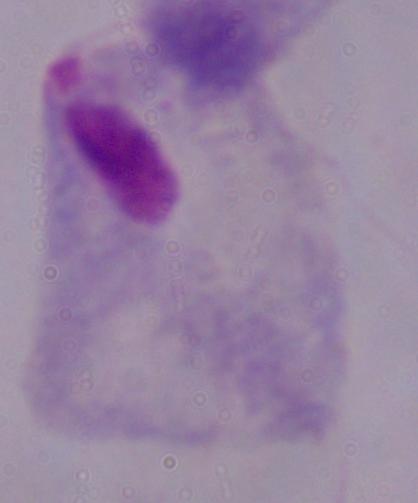
Summary:
  - Modality: photomicrograph
  - Magnification: 1000x
  - Identification: trichomonad